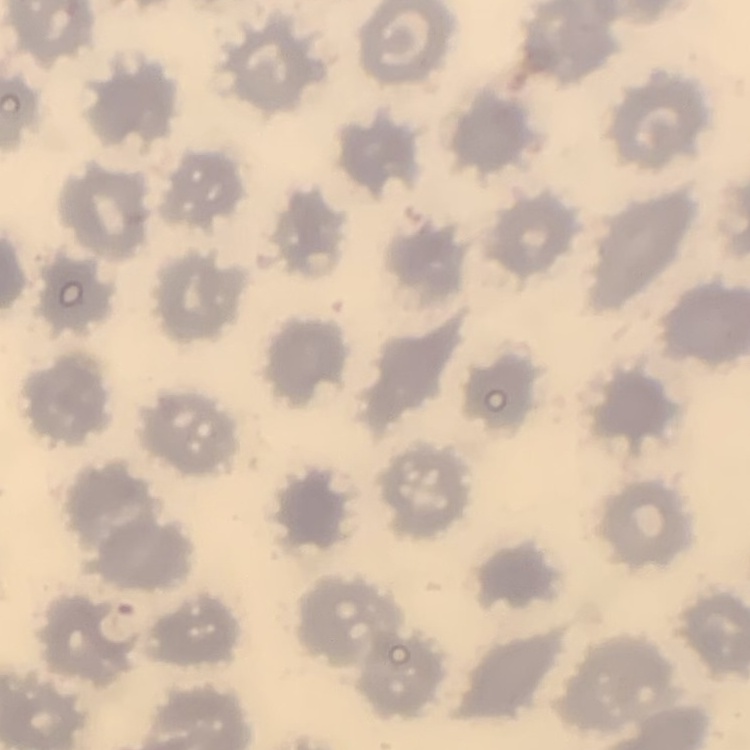
The erythrocytes exhibit no rouleaux formation. Thin blood film. One tile cut from a larger photomicrograph. Stained with either Field's or Giemsa.